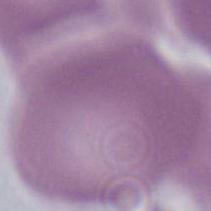 Micrograph. Captured at 1000x magnification. An erythrocyte is seen.